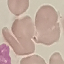

malaria status = uninfected
preparation = thin blood film
image type = cell patch, automatically extracted from a larger field of view and resized to 64 × 64 pixels
capture = smartphone camera at the microscope eyepiece
stain = Giemsa